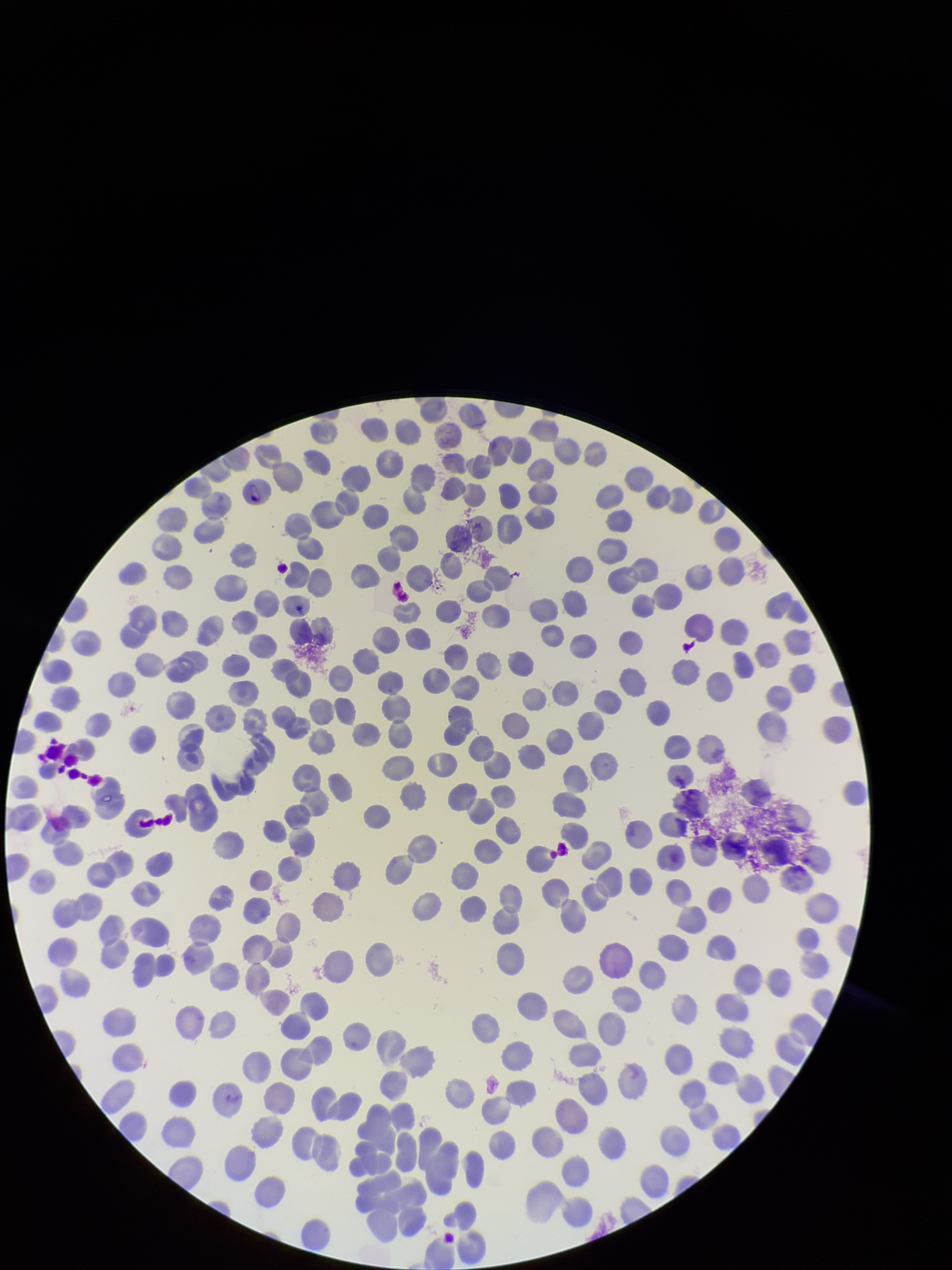

stain: Giemsa
species_reported_for_this_patient: Plasmodium vivax
field_of_view: single
preparation: thin smear
patient_malaria_status: positive
parasitized_red_blood_cells: detected
red_blood_cell_count: 245
parasitized_red_blood_cell_count: 1
image_size: 952×1270 pixels
capture: smartphone photograph through the microscope eyepiece